Comment on the morphology of the erythrocytes.
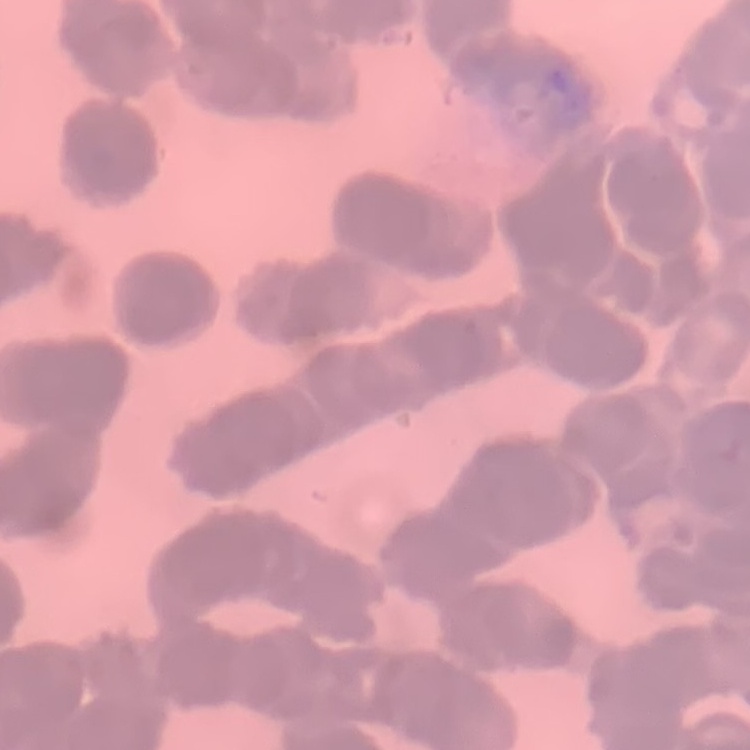
Rouleaux formation.

One tile cut from a larger photomicrograph. Thin blood film. Field's or Giemsa stain.